Classify this cell by malaria status.
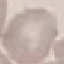

It is uninfected.

stain = Giemsa
image type = automatically extracted cell patch, resized to 64 × 64 pixels
preparation = thin smear
capture = smartphone camera at the microscope eyepiece